Locate every Plasmodium vivax-infected red blood cell.
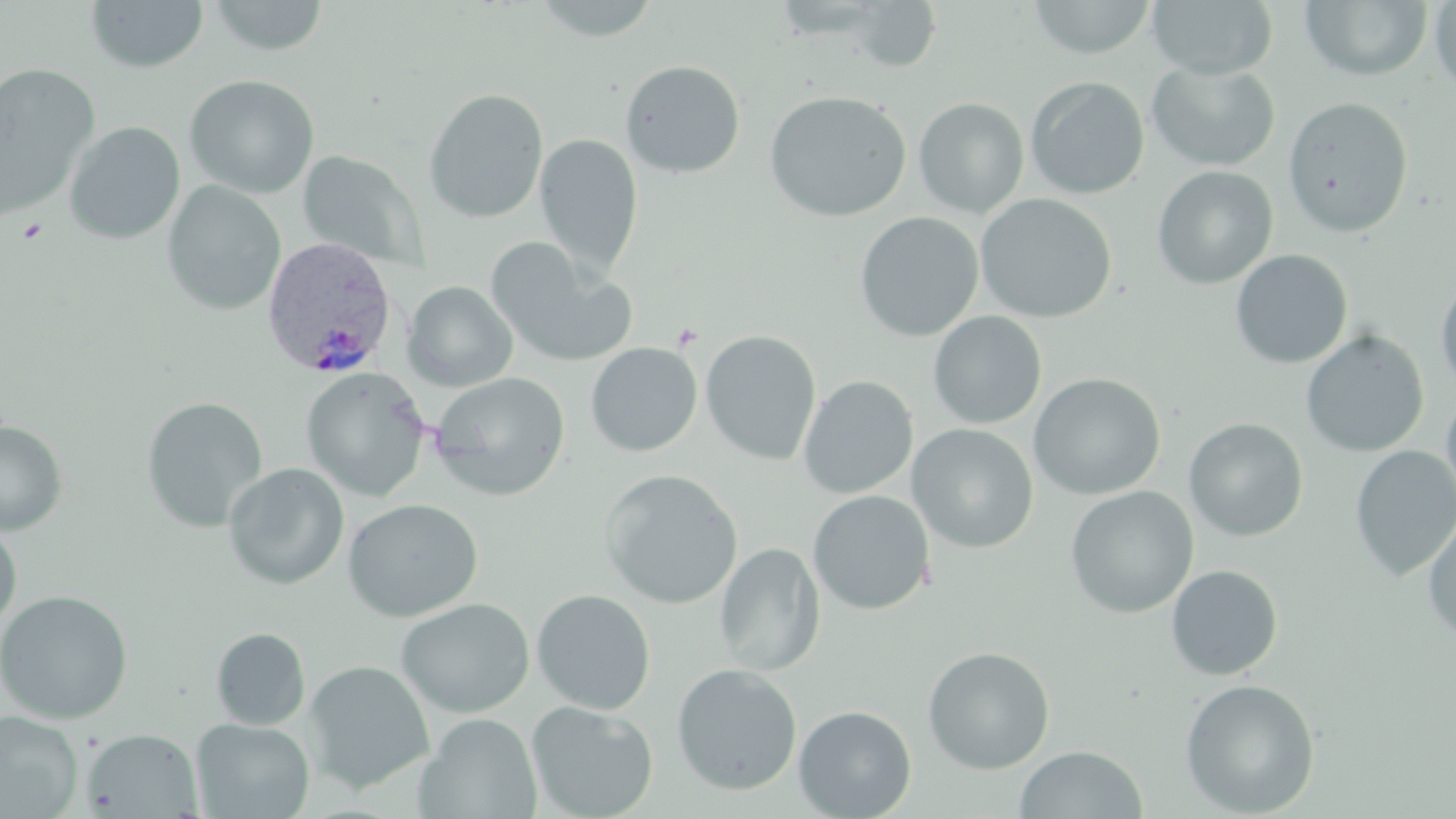
Approximate bounding boxes as (x1,y1)-(x2,y2) corner pairs in pixels.
Plasmodium vivax-infected red blood cells: (260,235)-(400,380).

Platelet locations: (15,217)-(48,244). Uninfected red blood cell locations: (207,0)-(330,57), (529,0)-(664,42), (1027,0)-(1158,59), (1146,0)-(1278,80), (1299,0)-(1434,82), (86,1)-(208,73), (1428,1)-(1456,98), (842,3)-(944,72), (620,60)-(746,178), (1146,61)-(1281,172), (0,63)-(100,218), (184,74)-(320,199), (1025,76)-(1150,199), (423,88)-(549,224), (763,91)-(912,222), (1282,96)-(1414,237), (913,97)-(1029,218), (64,121)-(185,244), (535,133)-(643,277), (298,150)-(427,271), (1151,166)-(1278,289), (162,180)-(286,316), (975,193)-(1117,323), (854,211)-(984,342), (484,238)-(637,368), (1229,249)-(1353,369), (1434,271)-(1456,397), (403,281)-(518,391), (927,311)-(1047,429), (700,330)-(822,465), (1300,330)-(1429,458), (585,342)-(703,457), (300,367)-(431,502), (428,371)-(571,502), (1028,373)-(1166,500), (798,375)-(919,499), (1440,388)-(1456,515), (141,396)-(267,532), (1184,418)-(1308,542), (0,420)-(68,535), (906,423)-(1039,553), (1350,445)-(1456,581), (222,462)-(350,590), (599,469)-(743,609), (1064,486)-(1199,618), (807,490)-(935,615), (343,498)-(484,622), (1422,510)-(1456,647), (0,521)-(22,633), (715,542)-(825,676), (1166,564)-(1283,680), (0,589)-(133,725), (531,589)-(656,715), (397,598)-(535,718), (211,627)-(311,730), (922,646)-(1056,774), (304,660)-(434,794), (671,663)-(803,796), (1180,678)-(1321,817), (525,700)-(659,818), (794,705)-(917,818), (0,712)-(83,817), (415,713)-(542,819), (191,718)-(315,819), (83,728)-(202,817), (1014,745)-(1148,819). Slide-level diagnosis: Plasmodium vivax. Thin blood film. May-Grünwald-Giemsa stain. Image is 1456×819 pixels. Captured at 1000x magnification. One field of a larger specimen. Light microscopy.